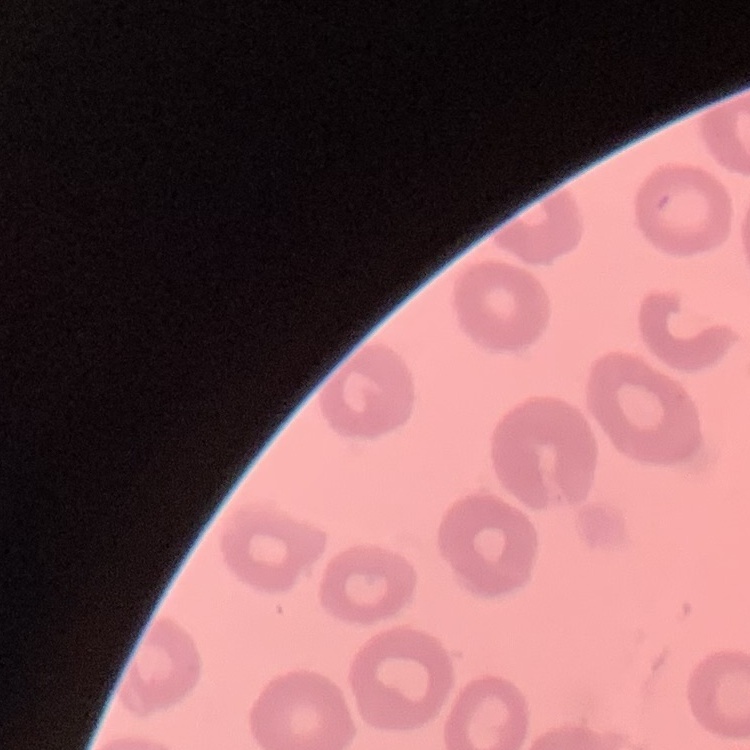

red_blood_cell_morphology: no rouleaux formation
stain: Field's or Giemsa
preparation: thin blood film
image_type: square crop of a larger photomicrograph